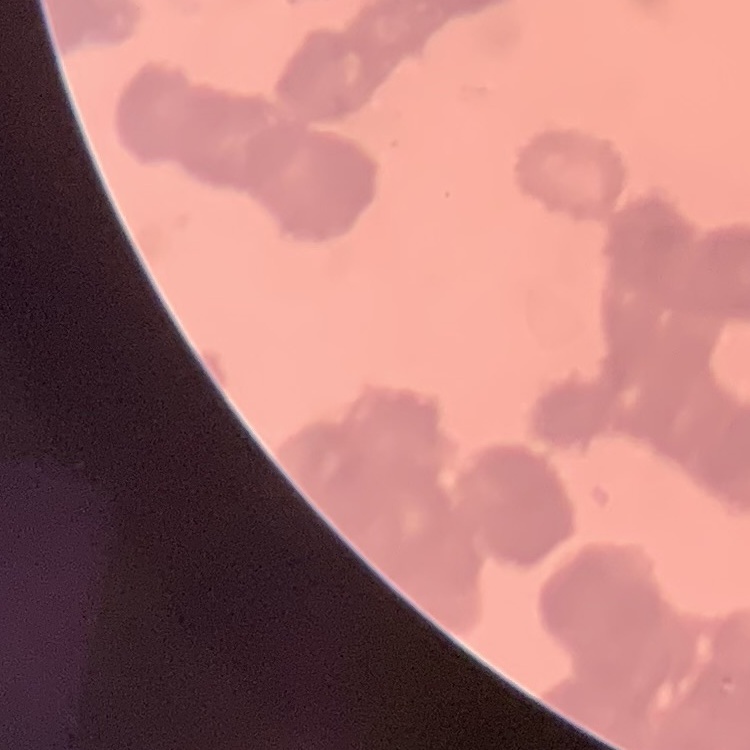
red blood cell morphology = rouleaux formation
image type = square crop of a larger photomicrograph
preparation = thin blood film
stain = Field's or Giemsa